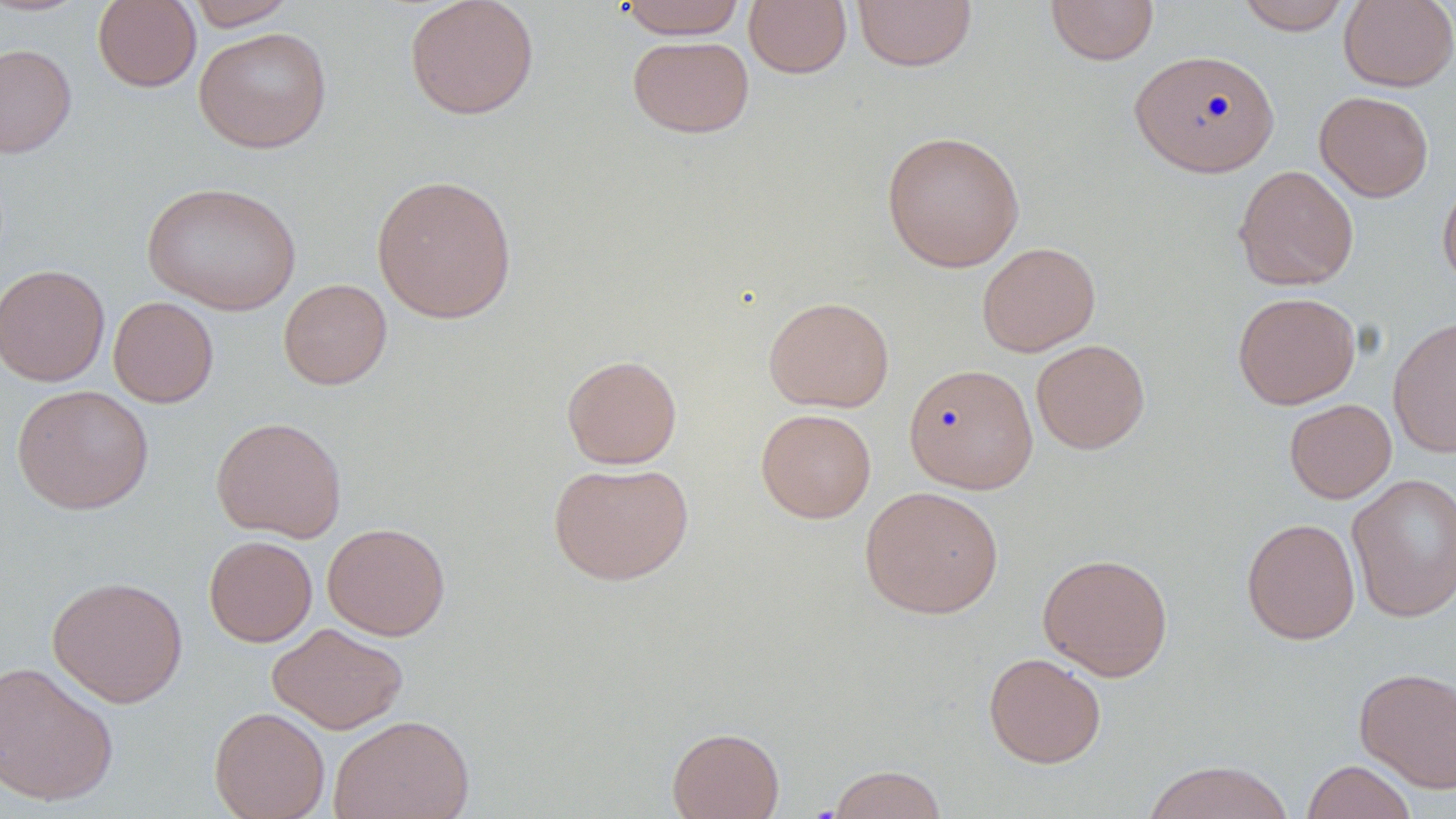
Summary:
  - Coordinate format: approximate bounding boxes as [x1, y1, x2, y2] in pixels
  - Uninfected red blood cell locations: [185, 0, 298, 30], [404, 0, 539, 120], [617, 0, 747, 39], [852, 0, 977, 72], [1045, 0, 1159, 65], [1236, 0, 1352, 35], [1338, 0, 1456, 92], [0, 1, 92, 16], [92, 1, 201, 92], [744, 1, 852, 78], [193, 27, 332, 153], [628, 35, 754, 138], [0, 43, 77, 157], [1129, 49, 1280, 177], [1314, 90, 1434, 202], [881, 130, 1026, 272], [1233, 165, 1359, 291], [371, 174, 518, 322], [1437, 174, 1456, 292], [141, 181, 303, 316], [977, 242, 1100, 356], [0, 263, 110, 387], [278, 278, 392, 390], [1232, 291, 1361, 409], [108, 296, 219, 407], [763, 296, 894, 413], [1388, 315, 1456, 458], [1031, 339, 1150, 454], [561, 354, 682, 469], [903, 363, 1038, 494], [12, 384, 154, 514], [1284, 399, 1396, 503], [755, 408, 876, 523], [211, 417, 347, 541], [548, 461, 694, 585], [1346, 473, 1456, 623], [860, 485, 1004, 619], [1241, 517, 1360, 645], [322, 522, 450, 640], [203, 535, 317, 646], [1037, 552, 1174, 680], [47, 574, 188, 707], [268, 622, 409, 735], [983, 652, 1107, 769], [0, 660, 120, 806], [1354, 666, 1456, 793], [209, 706, 330, 819], [329, 713, 475, 819], [667, 726, 785, 819], [1141, 759, 1296, 819], [1301, 759, 1416, 819], [826, 764, 948, 819]
  - Slide-level diagnosis: negative for blood parasites
  - Stain: May-Grünwald-Giemsa
  - Modality: optical microscopy
  - Preparation: thin blood smear
  - Field of view: one of a larger specimen
  - Image size: 1456×819 pixels
  - Magnification: 1000x